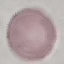
Summary:
  - Malaria status: uninfected
  - Stain: Giemsa
  - Image type: cell patch, automatically extracted from a larger field of view and resized to 64 × 64 pixels
  - Capture: smartphone through the microscope eyepiece
  - Preparation: thin blood smear